Comment on the morphology of the red blood cells.
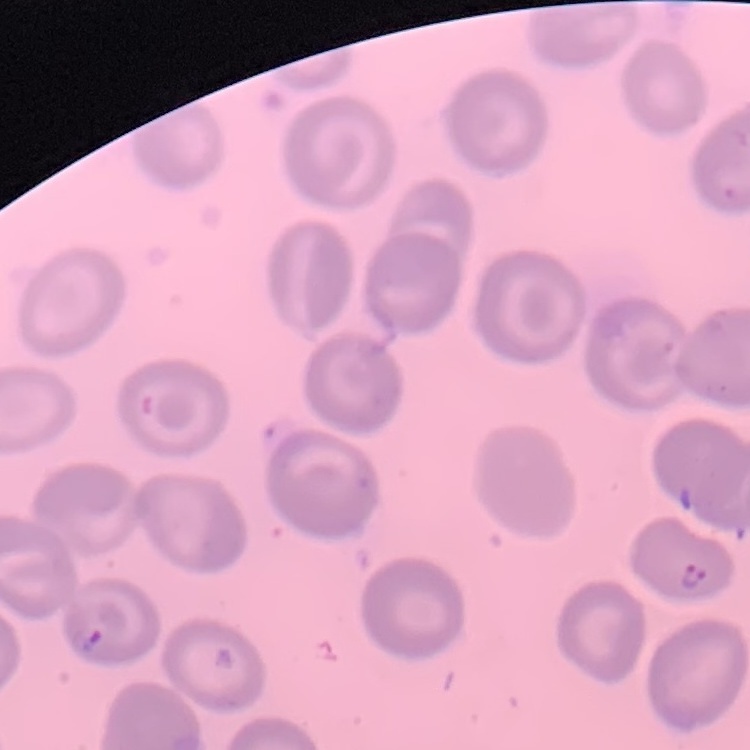

They show no rouleaux formation.

image type = square crop of a larger photomicrograph
preparation = thin peripheral smear
stain = Field's or Giemsa